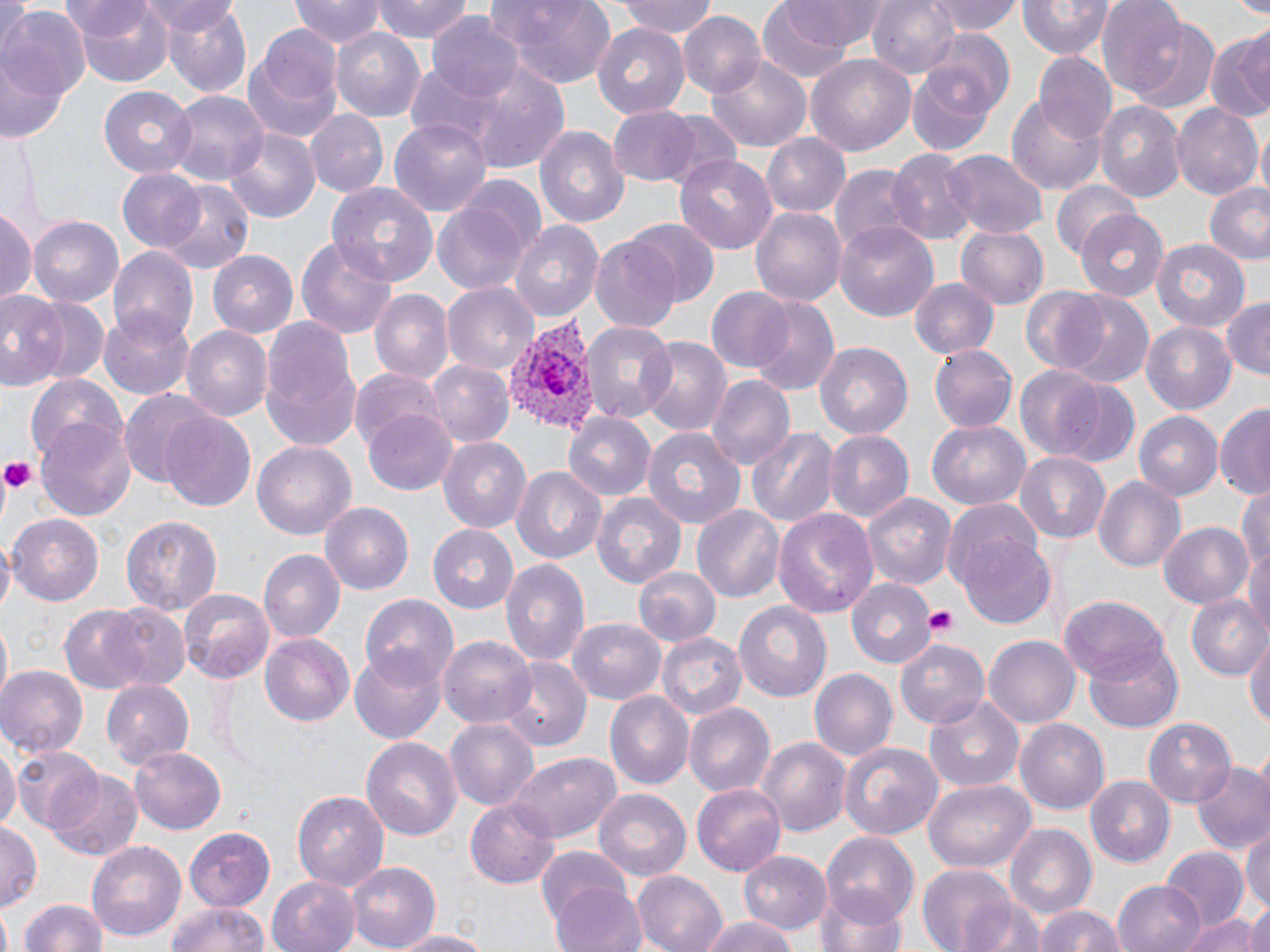

Summary:
  - Coordinate format: approximate bounding boxes as (x1, y1, x2, y2) in pixels
  - Plasmodium vivax-infected red blood cell locations: (500, 315, 599, 435)
  - Platelet locations: (0, 459, 37, 495), (923, 605, 960, 638)
  - Uninfected red blood cell locations: (63, 0, 175, 89), (293, 0, 384, 50), (371, 0, 474, 44), (619, 0, 722, 39), (867, 0, 960, 80), (928, 0, 1021, 38), (1019, 0, 1111, 60), (1095, 0, 1190, 95), (1231, 0, 1270, 15), (488, 1, 619, 89), (139, 2, 240, 40), (756, 3, 856, 83), (774, 3, 892, 50), (158, 4, 250, 101), (0, 7, 89, 108), (678, 12, 765, 99), (427, 15, 524, 102), (1126, 16, 1222, 112), (592, 25, 691, 120), (243, 26, 346, 146), (330, 27, 430, 124), (923, 30, 1014, 121), (1205, 30, 1270, 124), (806, 53, 917, 160), (1035, 53, 1114, 142), (707, 55, 813, 152), (906, 58, 1000, 156), (0, 64, 68, 146), (467, 64, 570, 174), (407, 66, 499, 147), (99, 85, 198, 178), (166, 92, 267, 190), (1007, 93, 1106, 195), (1093, 100, 1186, 203), (1171, 104, 1261, 200), (608, 107, 704, 186), (304, 110, 388, 198), (659, 110, 744, 190), (390, 117, 493, 219), (535, 125, 629, 229), (1253, 127, 1270, 199), (226, 130, 319, 223), (760, 134, 847, 216), (889, 149, 975, 245), (943, 151, 1045, 238), (674, 153, 778, 255), (829, 164, 924, 256), (116, 169, 209, 251), (453, 174, 550, 272), (1053, 180, 1142, 260), (156, 183, 253, 271), (329, 183, 438, 290), (1202, 183, 1270, 264), (431, 197, 533, 297), (749, 206, 846, 306), (0, 208, 35, 308), (1077, 210, 1169, 301), (30, 216, 124, 308), (508, 220, 603, 323), (624, 220, 721, 310), (835, 221, 939, 321), (957, 226, 1048, 308), (296, 234, 398, 340), (591, 235, 685, 332), (1150, 237, 1250, 330), (109, 248, 197, 347), (209, 250, 303, 336), (911, 279, 999, 359), (443, 282, 539, 376), (1019, 286, 1119, 377), (706, 287, 797, 373), (0, 289, 68, 390), (368, 289, 452, 384), (1052, 291, 1156, 389), (23, 295, 110, 387), (1220, 296, 1270, 379), (749, 297, 839, 398), (101, 311, 195, 400), (259, 317, 362, 454), (1140, 320, 1239, 417), (578, 321, 677, 424), (182, 326, 273, 421), (643, 338, 731, 437), (815, 341, 912, 442), (930, 345, 1017, 431), (425, 360, 513, 447), (1011, 365, 1105, 456), (351, 367, 453, 465), (1036, 375, 1142, 471), (709, 376, 795, 472), (25, 377, 127, 466), (119, 392, 217, 486), (1216, 403, 1270, 503), (362, 408, 459, 497), (1134, 411, 1223, 499), (160, 412, 256, 511), (563, 412, 656, 501), (36, 420, 137, 523), (927, 421, 1029, 510), (641, 425, 748, 527), (746, 425, 838, 531), (823, 430, 915, 524), (437, 437, 531, 535), (253, 442, 355, 540), (1015, 452, 1114, 545), (513, 465, 606, 562), (1092, 476, 1185, 571), (1236, 484, 1270, 577), (591, 491, 687, 585), (861, 492, 956, 593), (942, 499, 1044, 597), (321, 501, 415, 596), (691, 505, 784, 603), (771, 506, 879, 618), (7, 514, 104, 606), (121, 514, 223, 617), (1157, 520, 1257, 609), (428, 524, 517, 611), (958, 533, 1060, 631), (1244, 539, 1270, 637), (258, 549, 342, 643), (500, 556, 591, 672), (632, 565, 721, 647), (847, 578, 935, 669), (178, 587, 274, 681), (1187, 592, 1267, 679), (360, 593, 459, 690), (1060, 594, 1174, 685), (735, 602, 832, 701), (57, 604, 154, 693), (102, 606, 191, 692), (567, 617, 667, 704), (1, 621, 12, 702), (1245, 627, 1270, 734), (261, 633, 354, 727), (657, 633, 748, 722), (440, 635, 536, 728), (895, 635, 990, 728), (983, 637, 1078, 726), (1086, 642, 1184, 731), (349, 652, 448, 744), (505, 661, 590, 750), (0, 666, 87, 757), (808, 667, 896, 763), (103, 680, 194, 770), (606, 691, 694, 790), (924, 695, 1023, 791), (685, 702, 775, 798), (446, 717, 539, 810), (1016, 717, 1111, 815), (1144, 717, 1236, 805), (360, 736, 463, 840), (757, 737, 850, 839), (0, 740, 17, 840), (838, 740, 943, 841), (130, 746, 227, 833), (12, 748, 101, 832), (506, 750, 624, 843), (1190, 759, 1270, 856), (46, 769, 144, 860), (1085, 775, 1175, 868), (922, 778, 1035, 874), (692, 782, 787, 873), (293, 786, 388, 890), (593, 791, 691, 883), (466, 799, 559, 888), (0, 822, 41, 913), (1005, 822, 1096, 921), (183, 825, 279, 941), (1242, 825, 1270, 914), (820, 835, 921, 927), (87, 841, 187, 943), (1158, 846, 1247, 932), (535, 847, 634, 938), (740, 850, 832, 935), (345, 860, 440, 950), (916, 866, 1019, 950), (632, 870, 729, 952), (264, 874, 361, 952), (549, 880, 648, 952), (1114, 880, 1205, 952), (817, 889, 909, 952), (20, 896, 106, 952), (972, 900, 1046, 952), (163, 901, 272, 952), (1241, 901, 1270, 952), (1032, 904, 1133, 952), (1179, 910, 1263, 952), (698, 916, 796, 952), (385, 928, 496, 951)
  - Slide-level diagnosis: Plasmodium vivax
  - Magnification: 1000x
  - Modality: optical microscopy
  - Field of view: one of a larger specimen
  - Preparation: thin blood smear
  - Image size: 1270×952 pixels
  - Stain: May-Grünwald-Giemsa